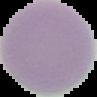

Summary:
  - Image type: cell region segmented out of the field of view; surrounding area masked to black
  - Result: negative for malaria parasites
  - Preparation: thin blood film
  - Image size: 97×97 pixels